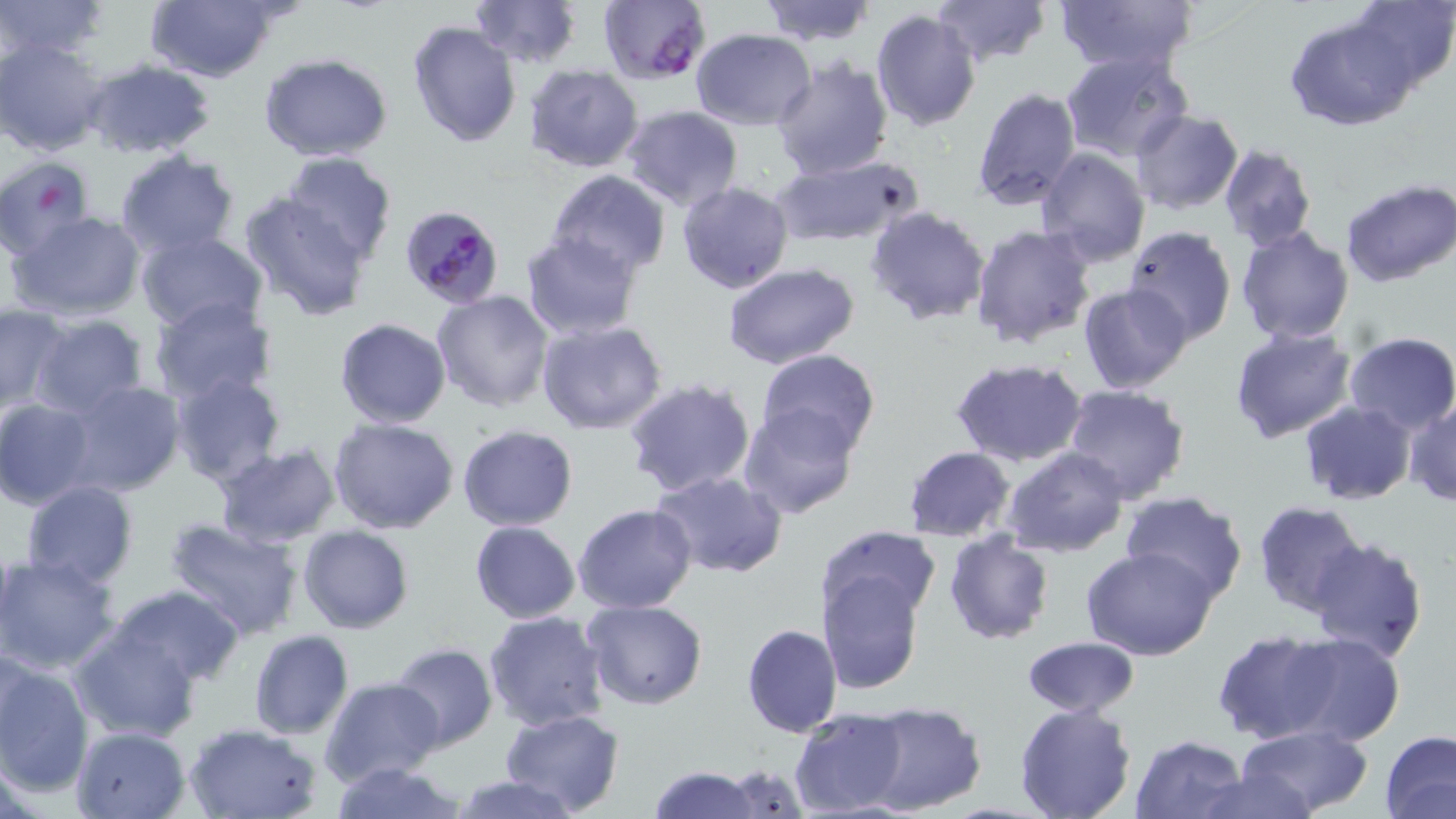

Summary:
  - Coordinate format: approximate bounding boxes as [x1, y1, x2, y2] in pixels
  - Plasmodium falciparum-infected red blood cell locations: [598, 0, 709, 85], [399, 206, 503, 305]
  - Uninfected red blood cell locations: [0, 0, 108, 60], [143, 0, 280, 82], [468, 0, 580, 68], [756, 0, 877, 46], [930, 0, 1050, 68], [1050, 0, 1200, 77], [1348, 1, 1456, 96], [870, 9, 980, 130], [1285, 14, 1416, 131], [407, 21, 522, 149], [690, 28, 815, 128], [0, 36, 108, 156], [1060, 50, 1191, 164], [259, 54, 394, 163], [770, 55, 892, 179], [79, 59, 219, 161], [524, 64, 644, 174], [1047, 74, 1174, 256], [970, 87, 1082, 210], [621, 106, 744, 211], [1130, 109, 1243, 215], [1217, 143, 1318, 252], [1035, 147, 1152, 267], [113, 150, 241, 259], [280, 153, 399, 269], [770, 153, 923, 248], [0, 155, 95, 259], [546, 169, 672, 276], [1341, 179, 1456, 288], [677, 182, 794, 296], [239, 191, 375, 320], [865, 205, 993, 326], [8, 211, 146, 321], [969, 224, 1096, 351], [1234, 225, 1355, 346], [1120, 226, 1236, 347], [136, 230, 268, 333], [522, 231, 642, 339], [722, 262, 860, 368], [1079, 284, 1194, 396], [431, 290, 556, 412], [150, 295, 279, 403], [0, 305, 70, 409], [28, 314, 150, 418], [333, 318, 452, 428], [535, 318, 668, 435], [1230, 324, 1358, 444], [1344, 331, 1456, 436], [754, 349, 880, 459], [948, 357, 1090, 467], [168, 372, 287, 489], [622, 379, 756, 499], [63, 382, 186, 498], [1059, 383, 1190, 503], [0, 398, 98, 510], [1405, 399, 1456, 507], [1298, 400, 1416, 505], [739, 404, 860, 518], [327, 417, 460, 536], [458, 424, 578, 530], [212, 444, 341, 548], [901, 446, 1015, 542], [1002, 447, 1129, 557], [649, 470, 786, 577], [20, 480, 139, 590], [1121, 491, 1247, 603], [1253, 501, 1368, 618], [573, 504, 697, 614], [164, 518, 305, 642], [469, 521, 580, 624], [298, 525, 414, 633], [817, 525, 941, 627], [943, 533, 1054, 644], [1308, 536, 1430, 665], [1082, 546, 1220, 660], [0, 553, 122, 675], [819, 572, 925, 695], [110, 584, 243, 685], [583, 599, 708, 710], [483, 611, 609, 730], [18, 623, 149, 765], [741, 623, 842, 737], [70, 624, 200, 740], [1212, 630, 1339, 744], [248, 631, 353, 740], [1281, 633, 1405, 747], [1022, 635, 1138, 718], [389, 643, 498, 751], [0, 656, 93, 797], [320, 676, 445, 787], [861, 702, 986, 816], [1014, 704, 1138, 819], [498, 708, 623, 816], [790, 708, 908, 817], [183, 721, 325, 819], [1234, 724, 1374, 818], [71, 725, 190, 819], [1381, 730, 1456, 818], [1130, 733, 1245, 818], [327, 763, 470, 819], [725, 763, 806, 818], [645, 764, 762, 819], [1195, 765, 1321, 819], [451, 775, 582, 819]
  - Slide-level diagnosis: Plasmodium falciparum
  - Magnification: 1000x
  - Stain: May-Grünwald-Giemsa
  - Field of view: single
  - Image size: 1456×819 pixels
  - Preparation: thin blood film
  - Modality: light microscopy